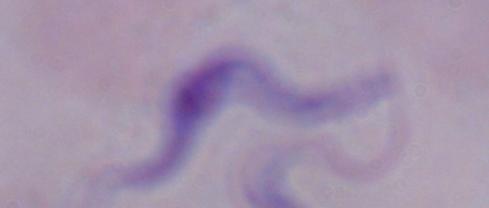
Summary:
  - Identification: trypanosome
  - Modality: photomicrograph
  - Magnification: 1000x